Report the malaria status of this cell.
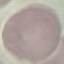
Uninfected.

Summary:
  - Stain: Giemsa
  - Preparation: thin blood smear
  - Capture: smartphone camera at the microscope eyepiece
  - Image type: automatically extracted cell patch, resized to 64 × 64 pixels